Identify the blood parasite species.
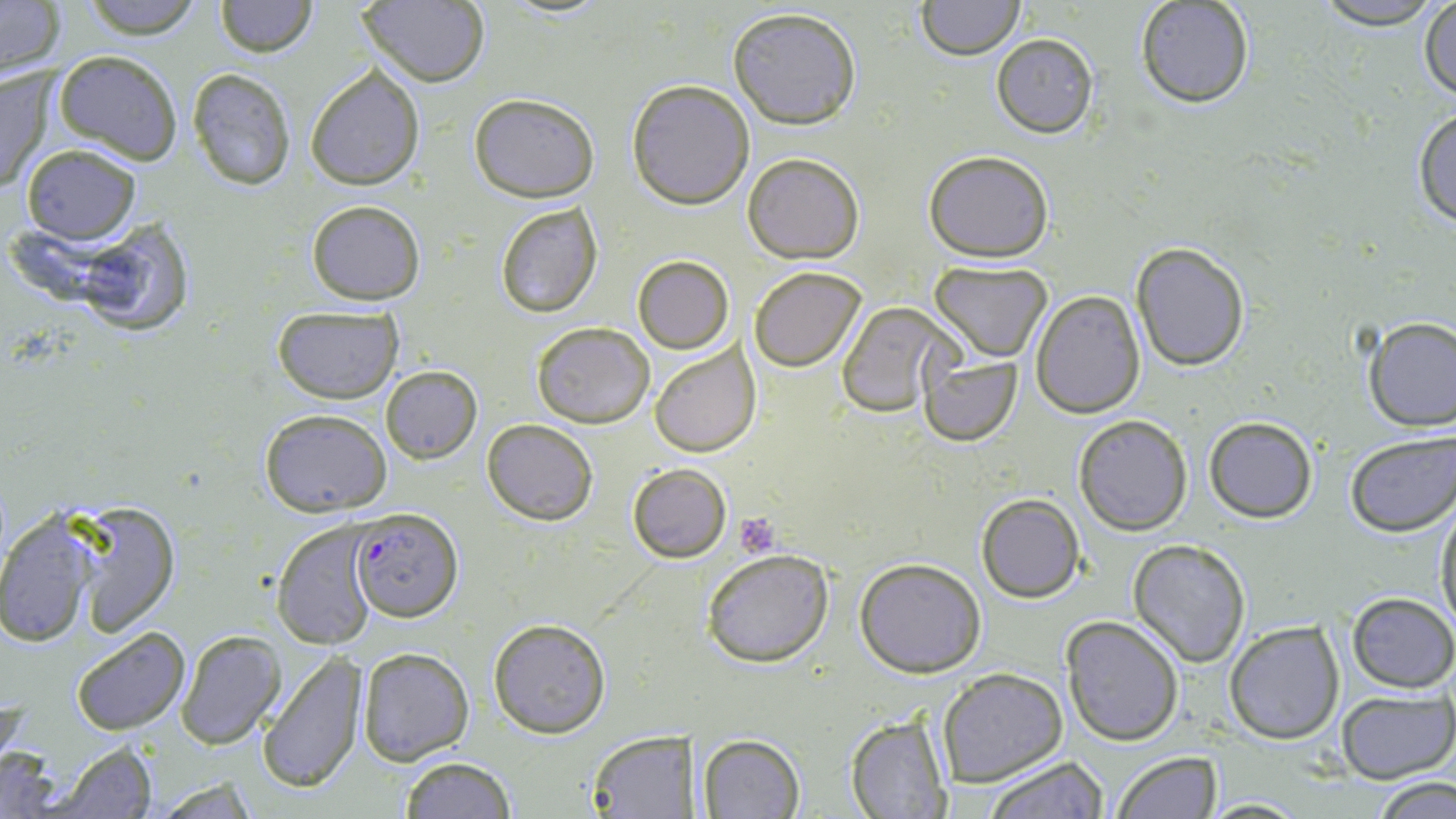
Plasmodium falciparum.

preparation = thin blood smear
uninfected red blood cell locations = approximate bounding boxes as [x1, y1, x2, y2] in pixels: [80, 0, 204, 40], [916, 0, 1024, 61], [1319, 0, 1434, 24], [0, 1, 67, 82], [213, 1, 317, 57], [356, 1, 490, 87], [1134, 1, 1256, 109], [1418, 2, 1456, 103], [728, 6, 862, 130], [991, 34, 1099, 138], [53, 50, 183, 165], [0, 66, 55, 197], [305, 66, 425, 190], [187, 68, 297, 189], [626, 79, 754, 209], [468, 93, 600, 203], [1411, 106, 1456, 227], [19, 143, 142, 245], [922, 149, 1054, 260], [743, 153, 864, 263], [493, 199, 603, 318], [307, 200, 425, 305], [65, 216, 195, 334], [1131, 242, 1250, 370], [632, 255, 734, 354], [929, 259, 1052, 360], [749, 265, 866, 371], [1030, 290, 1144, 417], [835, 300, 956, 418], [271, 304, 404, 403], [1360, 316, 1456, 432], [531, 322, 654, 428], [647, 342, 757, 458], [917, 353, 1023, 445], [380, 364, 482, 464], [258, 407, 393, 517], [1073, 414, 1192, 535], [1203, 416, 1318, 523], [482, 419, 597, 526], [1344, 432, 1456, 536], [626, 463, 732, 563], [977, 495, 1083, 602], [66, 500, 181, 634], [1434, 502, 1456, 637], [0, 512, 101, 649], [272, 519, 384, 650], [1127, 539, 1251, 667], [702, 547, 834, 668], [855, 558, 985, 677], [1346, 592, 1455, 693], [1059, 615, 1184, 745], [487, 616, 611, 738], [1223, 619, 1344, 744], [72, 629, 190, 736], [175, 630, 285, 749], [356, 647, 476, 766], [258, 653, 370, 794], [938, 668, 1067, 787], [1337, 689, 1455, 784], [846, 714, 953, 819], [586, 729, 696, 816], [697, 733, 805, 817], [44, 741, 160, 818], [0, 748, 64, 817], [1112, 751, 1221, 819], [397, 755, 518, 819], [980, 755, 1108, 818], [1368, 776, 1456, 819], [1200, 795, 1309, 816]
Plasmodium falciparum-infected red blood cell locations = approximate bounding boxes as [x1, y1, x2, y2] in pixels: [349, 507, 460, 624]
modality = light microscopy
stain = May-Grünwald-Giemsa
magnification = 1000x
image size = 1456×819 pixels
platelet locations = approximate bounding boxes as [x1, y1, x2, y2] in pixels: [732, 512, 780, 558]
field of view = single